Locate every Plasmodium falciparum-infected red blood cell.
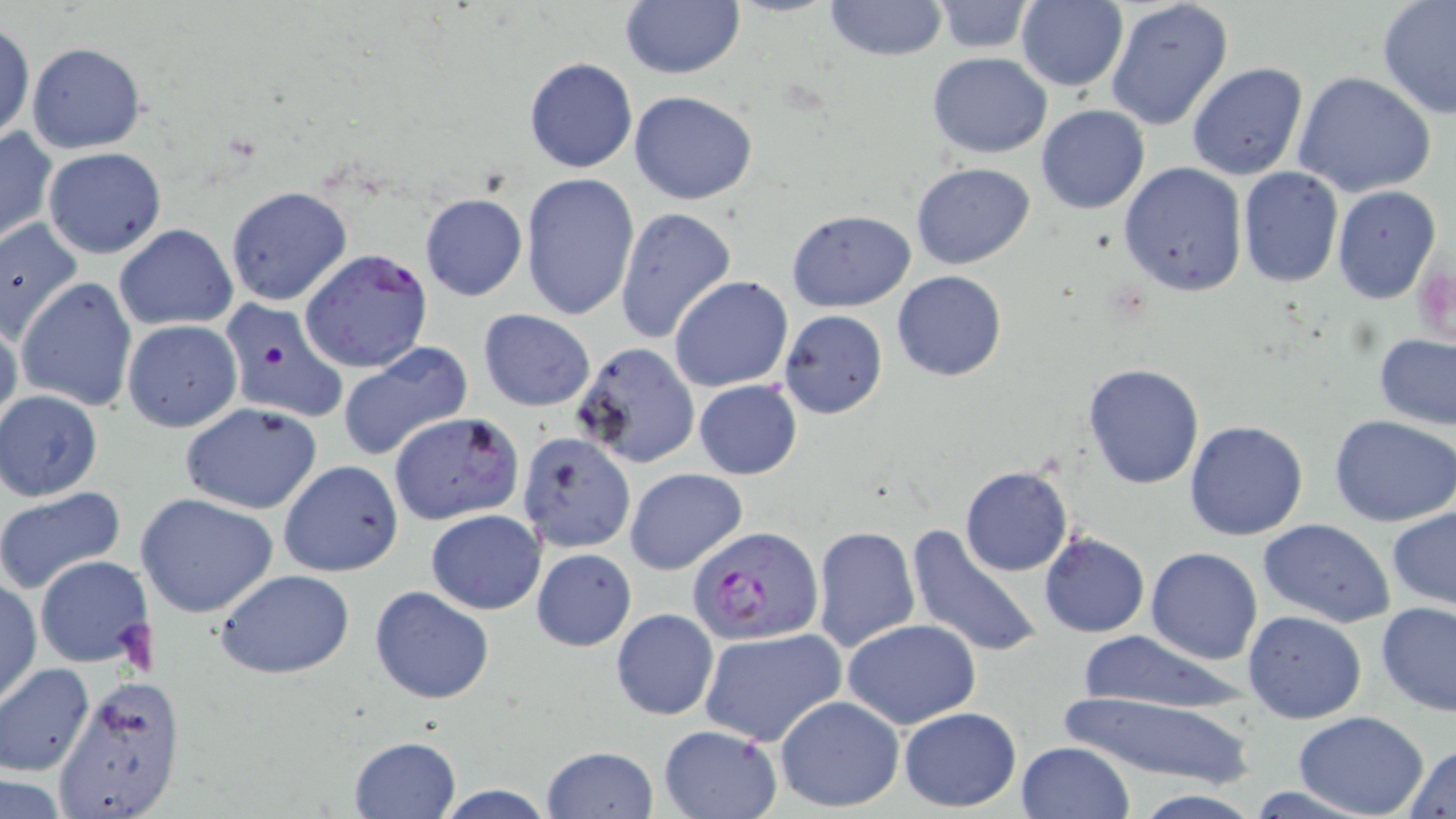
Approximate bounding boxes as [x1, y1, x2, y2] in pixels.
Plasmodium falciparum-infected red blood cells: [300, 248, 434, 373], [686, 524, 824, 645].

Uninfected red blood cell locations: [619, 0, 744, 79], [1105, 0, 1235, 132], [822, 1, 949, 61], [1014, 1, 1129, 90], [1377, 1, 1456, 120], [932, 2, 1037, 53], [0, 18, 35, 145], [26, 43, 146, 153], [927, 52, 1052, 158], [523, 55, 638, 173], [1186, 62, 1309, 182], [1292, 70, 1436, 199], [629, 91, 759, 206], [1036, 104, 1150, 214], [0, 124, 57, 249], [43, 147, 166, 259], [911, 161, 1035, 270], [1119, 161, 1247, 297], [1238, 167, 1343, 287], [520, 172, 640, 322], [1331, 184, 1442, 303], [225, 186, 353, 308], [419, 192, 527, 301], [615, 206, 737, 344], [787, 210, 915, 311], [0, 219, 84, 343], [115, 223, 239, 330], [892, 270, 1006, 381], [669, 275, 794, 392], [16, 277, 138, 411], [217, 297, 349, 426], [479, 309, 595, 411], [779, 309, 888, 420], [0, 313, 22, 439], [122, 320, 242, 431], [1374, 332, 1456, 431], [338, 340, 473, 463], [572, 342, 699, 468], [1083, 363, 1205, 489], [694, 379, 802, 479], [1, 391, 103, 499], [179, 401, 324, 515], [388, 412, 524, 525], [1330, 415, 1456, 526], [1185, 419, 1309, 540], [517, 432, 636, 552], [278, 459, 403, 576], [960, 465, 1074, 576], [625, 467, 747, 575], [0, 484, 127, 594], [136, 491, 279, 618], [1387, 507, 1456, 613], [425, 509, 544, 613], [1259, 518, 1396, 628], [907, 524, 1044, 660], [811, 525, 919, 654], [1041, 534, 1150, 637], [531, 547, 637, 651], [1146, 547, 1263, 665], [34, 555, 155, 668], [214, 570, 355, 678], [1, 577, 41, 705], [369, 585, 494, 703], [1377, 601, 1456, 716], [612, 608, 718, 720], [1242, 611, 1367, 724], [842, 619, 981, 728], [698, 627, 845, 747], [1076, 630, 1248, 716], [0, 663, 94, 775], [52, 676, 187, 819], [1058, 691, 1255, 785], [775, 694, 905, 814], [897, 707, 1020, 811], [1294, 713, 1429, 818], [657, 724, 782, 818], [348, 736, 462, 819], [1016, 740, 1134, 819], [1406, 743, 1456, 818], [540, 745, 658, 819], [1, 776, 73, 816], [430, 784, 560, 818], [1127, 791, 1267, 818]. Slide-level diagnosis: Plasmodium falciparum. Light microscopy. Captured at 1000x magnification. May-Grünwald-Giemsa-stained preparation. One field of a larger specimen. Image is 1456×819 pixels. Thin blood smear.